Locate and identify every blood parasite.
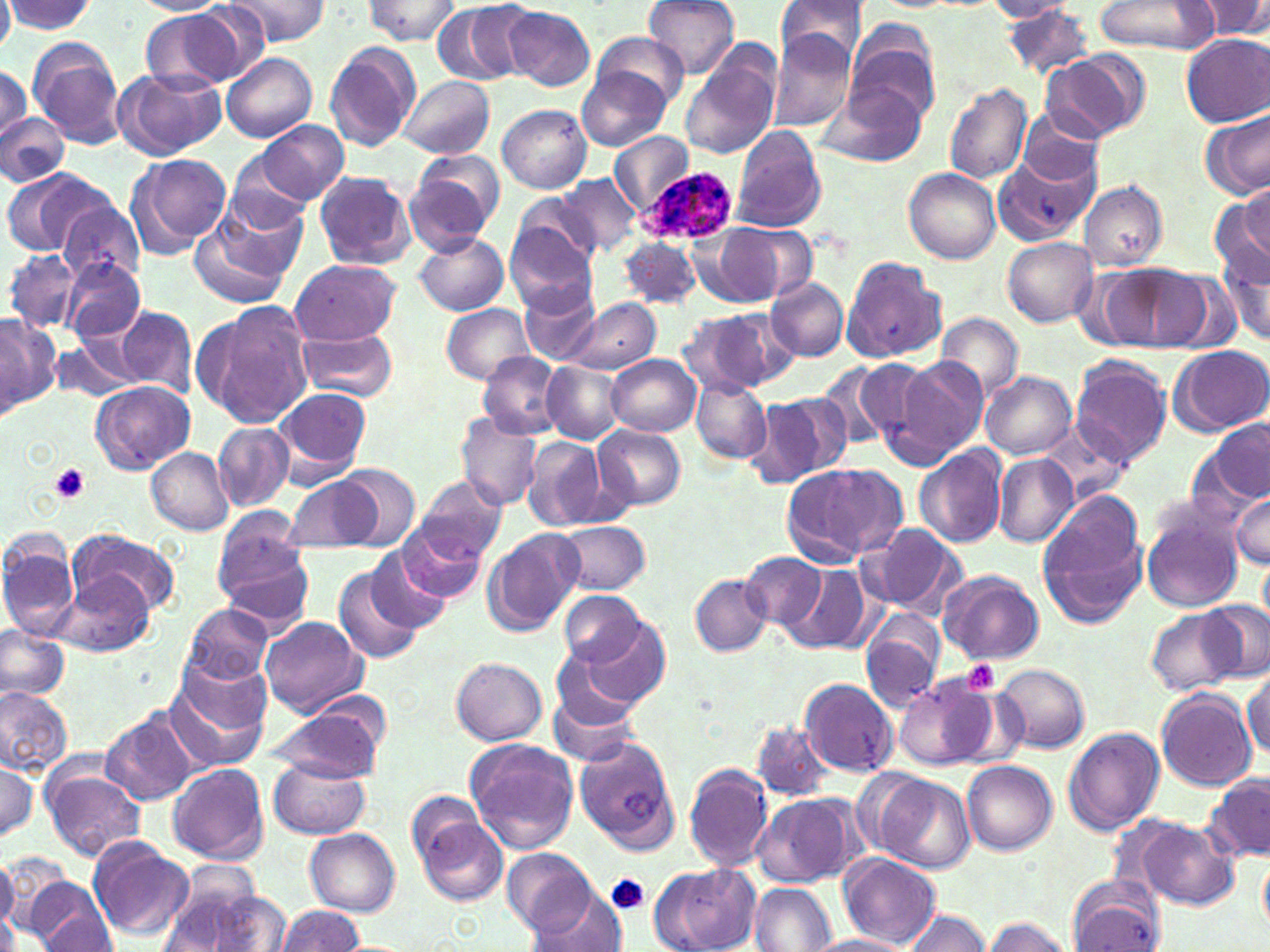

Approximate bounding boxes as [x1, y1, x2, y2] in pixels.
Plasmodium ovale-infected red blood cells: [642, 162, 738, 246].
No Plasmodium falciparum, Plasmodium malariae, Plasmodium vivax, Babesia divergens, or Trypanosoma brucei observed.

slide_level_diagnosis: Plasmodium ovale
preparation: thin blood smear
uninfected_red_blood_cell_locations: 'approximate bounding boxes as [x1, y1, x2, y2] in pixels: [0, 0, 15, 56], [133, 0, 230, 15], [223, 0, 326, 48], [365, 0, 459, 44], [431, 0, 532, 85], [646, 0, 740, 77], [774, 0, 869, 69], [1191, 0, 1270, 40], [2, 1, 98, 36], [983, 1, 1077, 21], [1093, 1, 1217, 55], [177, 3, 272, 84], [501, 5, 596, 91], [1001, 6, 1098, 79], [142, 10, 240, 90], [592, 32, 691, 106], [767, 32, 858, 130], [849, 32, 941, 123], [1181, 34, 1270, 126], [27, 38, 126, 149], [325, 40, 420, 153], [680, 48, 781, 161], [1041, 52, 1144, 144], [222, 53, 317, 142], [578, 64, 670, 152], [0, 65, 30, 145], [116, 68, 224, 160], [400, 74, 494, 160], [825, 81, 929, 168], [944, 82, 1032, 184], [498, 105, 591, 194], [1016, 108, 1107, 190], [1199, 109, 1269, 200], [0, 112, 68, 188], [250, 119, 349, 206], [731, 126, 826, 234], [610, 132, 693, 214], [127, 154, 232, 258], [993, 154, 1095, 247], [404, 155, 502, 255], [2, 167, 104, 256], [904, 169, 1001, 265], [314, 172, 417, 269], [557, 175, 642, 257], [1241, 180, 1269, 259], [1079, 181, 1168, 270], [1214, 188, 1270, 292], [215, 191, 310, 283], [514, 193, 603, 270], [56, 198, 146, 285], [503, 213, 601, 313], [188, 216, 295, 312], [711, 221, 815, 306], [414, 233, 509, 315], [1002, 237, 1098, 325], [621, 238, 701, 307], [4, 250, 82, 334], [1219, 253, 1269, 347], [842, 254, 946, 364], [61, 256, 145, 343], [289, 259, 401, 345], [1103, 263, 1207, 349], [765, 277, 848, 361], [520, 283, 600, 363], [566, 298, 659, 374], [192, 301, 316, 429], [440, 303, 537, 385], [116, 304, 196, 396], [674, 312, 778, 399], [933, 313, 1023, 403], [0, 314, 59, 417], [300, 327, 399, 402], [52, 335, 144, 403], [1168, 344, 1270, 435], [477, 352, 565, 438], [607, 355, 701, 436], [853, 356, 941, 457], [1070, 356, 1170, 468], [893, 357, 987, 460], [541, 361, 625, 444], [814, 363, 893, 453], [982, 372, 1076, 459], [689, 378, 772, 463], [92, 381, 194, 474], [275, 385, 374, 482], [757, 393, 851, 484], [455, 412, 544, 513], [1040, 419, 1129, 507], [1207, 420, 1270, 503], [214, 423, 293, 510], [595, 424, 686, 510], [521, 435, 607, 532], [915, 446, 1007, 548], [148, 448, 234, 534], [993, 455, 1078, 547], [781, 463, 906, 565], [336, 464, 419, 549], [284, 475, 380, 551], [415, 476, 508, 561], [1036, 489, 1147, 632], [1231, 492, 1269, 569], [1140, 500, 1246, 613], [556, 520, 651, 595], [397, 522, 487, 603], [857, 522, 967, 618], [211, 525, 313, 628], [483, 528, 586, 637], [67, 530, 179, 620], [0, 532, 82, 641], [362, 549, 452, 634], [742, 550, 827, 630], [1259, 557, 1270, 626], [332, 563, 426, 665], [783, 564, 871, 654], [939, 570, 1045, 666], [56, 572, 155, 657], [689, 574, 773, 656], [558, 591, 644, 668], [1200, 601, 1269, 684], [181, 603, 272, 685], [1146, 607, 1245, 695], [859, 609, 947, 713], [258, 616, 367, 717], [578, 616, 673, 709], [0, 625, 69, 704], [551, 647, 644, 732], [451, 657, 547, 746], [994, 663, 1090, 753], [164, 671, 272, 773], [1244, 671, 1269, 759], [894, 674, 996, 771], [801, 678, 898, 776], [0, 684, 72, 776], [549, 687, 644, 768], [1156, 689, 1256, 791], [267, 704, 386, 782], [100, 710, 197, 806], [752, 722, 837, 801], [1063, 726, 1165, 836], [575, 737, 681, 855], [463, 738, 578, 853], [0, 759, 40, 846], [269, 759, 370, 839], [961, 759, 1056, 854], [684, 761, 774, 873], [168, 763, 269, 864], [43, 769, 146, 862], [870, 774, 976, 874], [1204, 776, 1270, 863], [751, 792, 860, 888], [414, 808, 508, 907], [1135, 819, 1240, 910], [306, 827, 401, 916], [88, 838, 195, 939], [503, 848, 594, 937], [837, 853, 942, 948], [0, 857, 19, 932], [1259, 857, 1270, 934], [649, 863, 761, 952], [159, 869, 274, 952], [1065, 875, 1163, 951], [26, 880, 116, 952], [750, 882, 836, 952], [526, 889, 630, 952], [276, 905, 367, 952], [899, 910, 992, 952], [36, 915, 118, 949], [981, 916, 1075, 952], [809, 934, 914, 952]'
stain: May-Grünwald-Giemsa
magnification: 1000x
platelet_locations: 'approximate bounding boxes as [x1, y1, x2, y2] in pixels: [50, 464, 89, 504], [962, 661, 1000, 694], [606, 873, 649, 915]'
image_size: 1270×952 pixels
field_of_view: single
modality: optical microscopy